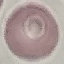
result = no malaria parasites detected
capture = smartphone camera at the microscope eyepiece
image type = automatically extracted cell patch, resized to 64 × 64 pixels
preparation = thin blood smear
stain = Giemsa